Locate every blood parasite and identify its species.
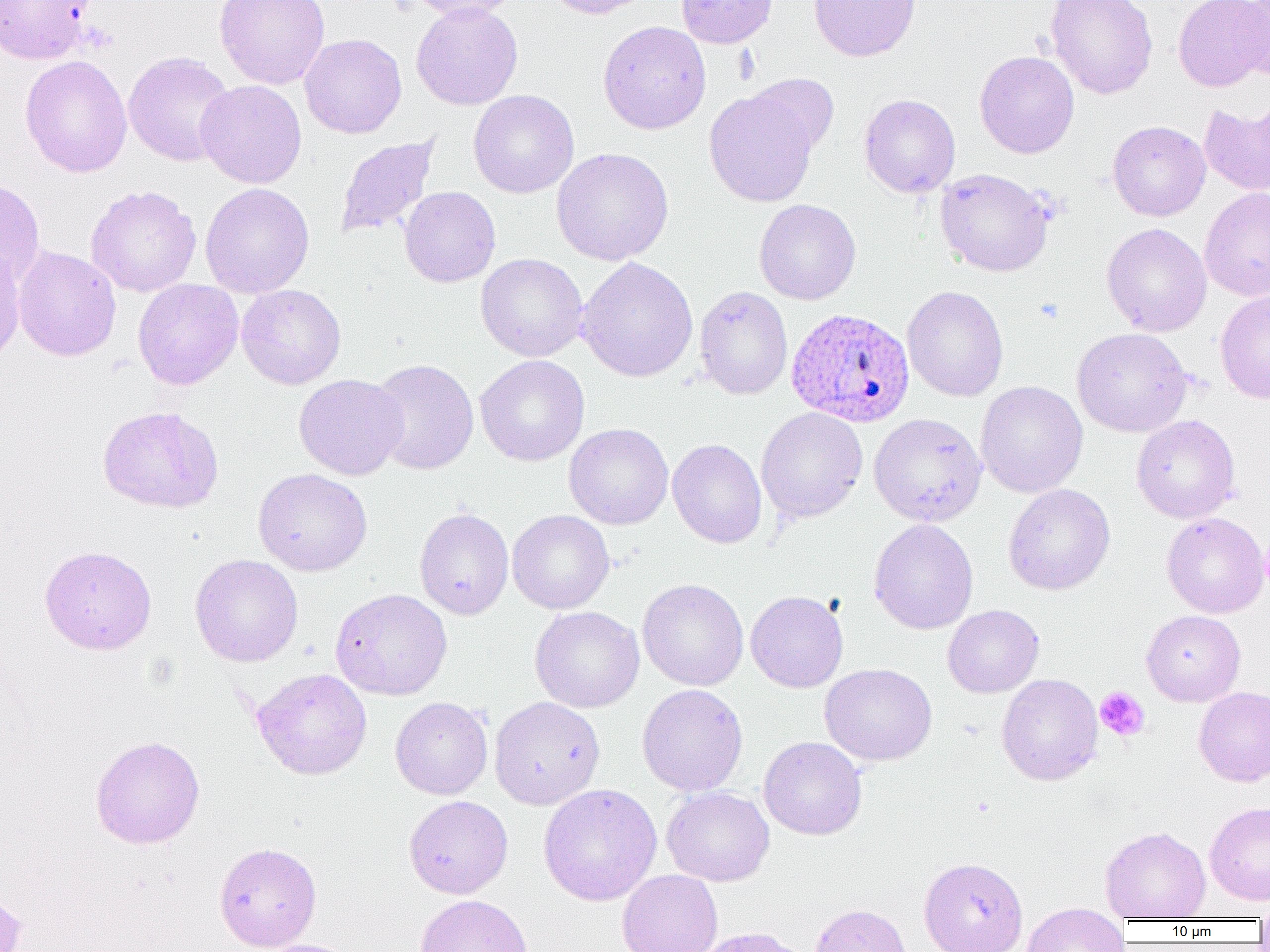
Approximate bounding boxes as (x1, y1, x2, y2) in pixels.
Plasmodium ovale-infected red blood cells: (786, 308, 915, 428).
No Plasmodium falciparum, Plasmodium malariae, Plasmodium vivax, Babesia divergens, or Trypanosoma brucei observed.

Platelet locations: (1094, 686, 1150, 742). Uninfected red blood cell locations: (0, 0, 95, 64), (214, 0, 331, 90), (404, 0, 524, 20), (543, 0, 655, 19), (676, 0, 778, 49), (808, 0, 921, 62), (1043, 0, 1158, 99), (1173, 0, 1268, 92), (410, 1, 524, 110), (1236, 1, 1270, 81), (598, 20, 711, 134), (299, 33, 407, 138), (122, 51, 236, 167), (974, 51, 1079, 158), (19, 55, 132, 177), (746, 72, 839, 157), (196, 80, 307, 188), (468, 89, 579, 198), (704, 89, 819, 207), (859, 93, 960, 198), (1199, 103, 1270, 197), (1107, 120, 1210, 221), (335, 135, 441, 240), (551, 147, 674, 266), (934, 168, 1055, 277), (0, 177, 46, 288), (200, 182, 315, 298), (85, 185, 201, 297), (399, 187, 501, 288), (1199, 187, 1270, 302), (754, 199, 861, 305), (1101, 222, 1212, 337), (0, 244, 25, 367), (12, 245, 121, 362), (475, 253, 588, 361), (577, 256, 698, 382), (133, 279, 243, 390), (236, 284, 346, 389), (694, 286, 793, 400), (901, 286, 1009, 402), (1215, 290, 1270, 403), (1071, 327, 1193, 437), (474, 354, 589, 466), (368, 358, 479, 475), (294, 374, 408, 480), (975, 381, 1088, 498), (97, 405, 225, 513), (755, 407, 868, 524), (868, 413, 987, 526), (1131, 414, 1240, 523), (563, 422, 674, 529), (668, 438, 767, 548), (253, 468, 373, 576), (1003, 483, 1115, 595), (414, 507, 514, 620), (507, 510, 614, 614), (1161, 512, 1269, 618), (868, 518, 979, 634), (39, 545, 157, 654), (189, 554, 303, 666), (638, 578, 749, 691), (330, 588, 452, 700), (745, 590, 848, 692), (943, 604, 1044, 697), (530, 606, 645, 713), (1141, 610, 1246, 706), (820, 663, 937, 766), (251, 667, 372, 780), (996, 673, 1103, 785), (637, 684, 748, 796), (1193, 686, 1270, 786), (390, 696, 493, 799), (489, 696, 605, 809), (90, 735, 205, 849), (758, 736, 867, 840), (538, 783, 662, 906), (661, 786, 774, 886), (404, 795, 513, 899), (1205, 801, 1270, 905), (1100, 826, 1211, 921), (214, 841, 322, 951), (918, 857, 1028, 952), (617, 870, 723, 952), (0, 889, 28, 952), (415, 894, 533, 952), (1254, 900, 1270, 927), (1021, 902, 1129, 952), (809, 903, 913, 952), (255, 938, 360, 952). Slide-level diagnosis: Plasmodium ovale. Image is 1270×952 pixels. Thin blood film. Optical microscopy. Captured at 1000x magnification. One field of a larger specimen.